Name the parasite shown.
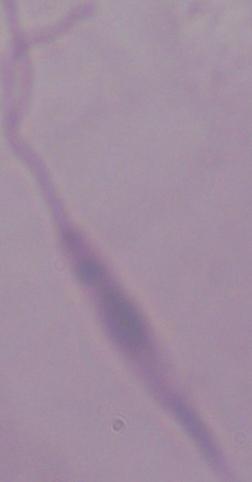

This is Leishmania.

modality = photomicrograph
magnification = 1000x